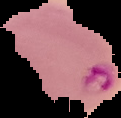

Image is 121×118 pixels. From a thin blood smear. Result: malaria parasites identified. Segmented cell region on a black background.